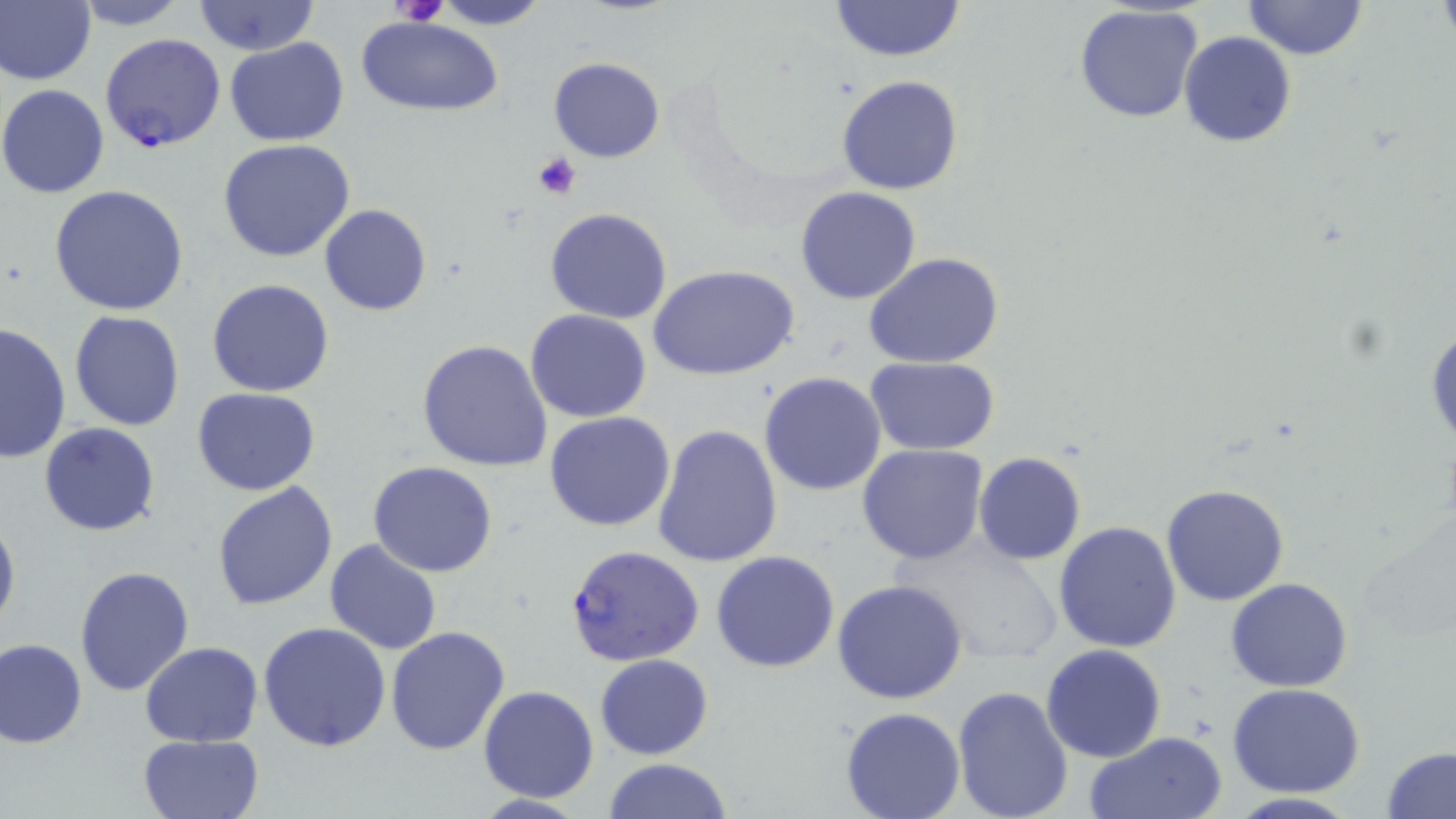
slide-level diagnosis = Plasmodium falciparum
uninfected red blood cell locations = approximate bounding boxes as [x1, y1, x2, y2] in pixels: [0, 0, 96, 87], [70, 0, 191, 29], [430, 0, 549, 29], [829, 0, 966, 63], [1242, 0, 1367, 61], [193, 1, 319, 55], [1074, 5, 1207, 126], [355, 15, 505, 116], [1179, 31, 1296, 147], [224, 38, 349, 147], [548, 56, 665, 164], [836, 74, 964, 195], [0, 84, 113, 198], [218, 139, 357, 263], [48, 186, 191, 317], [795, 186, 923, 305], [318, 204, 432, 315], [544, 207, 673, 324], [864, 253, 1006, 368], [650, 264, 799, 382], [207, 278, 335, 397], [526, 308, 652, 422], [68, 312, 185, 431], [1425, 314, 1456, 450], [0, 321, 71, 463], [417, 340, 554, 472], [866, 357, 998, 454], [759, 371, 888, 495], [192, 387, 323, 495], [543, 411, 676, 532], [39, 422, 160, 536], [651, 424, 783, 568], [857, 444, 989, 565], [974, 452, 1087, 564], [368, 461, 498, 578], [212, 480, 339, 611], [1161, 483, 1290, 605], [0, 507, 20, 639], [1054, 522, 1181, 652], [887, 535, 1069, 668], [323, 539, 442, 655], [711, 551, 840, 672], [75, 565, 195, 697], [1226, 576, 1351, 692], [832, 579, 967, 704], [258, 622, 392, 753], [385, 626, 510, 754], [0, 638, 87, 748], [140, 641, 264, 747], [1041, 644, 1167, 764], [594, 653, 714, 759], [953, 683, 1074, 818], [1227, 683, 1366, 798], [479, 685, 600, 802], [838, 707, 967, 819], [1084, 732, 1227, 818], [138, 734, 263, 818], [1380, 745, 1455, 819], [603, 758, 733, 818]
image size = 1456×819 pixels
stain = May-Grünwald-Giemsa
modality = light microscopy
preparation = thin blood smear
platelet locations = approximate bounding boxes as [x1, y1, x2, y2] in pixels: [393, 0, 449, 28], [531, 151, 583, 200]
magnification = 1000x
field of view = one of a larger specimen
Plasmodium falciparum-infected red blood cell locations = approximate bounding boxes as [x1, y1, x2, y2] in pixels: [100, 31, 225, 153], [563, 544, 706, 668]